Describe the morphology of the erythrocytes.
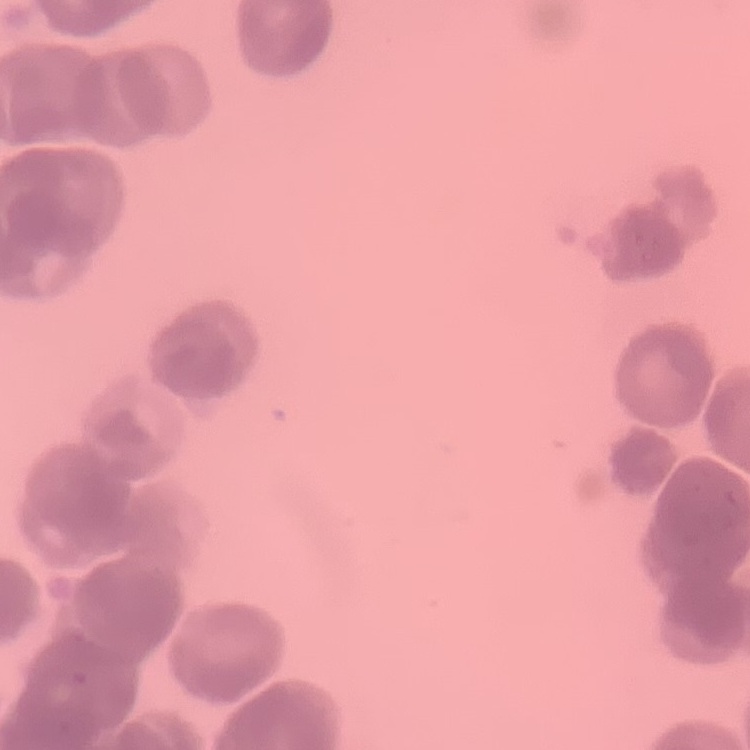
They show rouleaux formation.

Summary:
  - Preparation: thin blood film
  - Image type: one tile cut from a larger photomicrograph
  - Stain: Field's or Giemsa